Name the parasite shown.
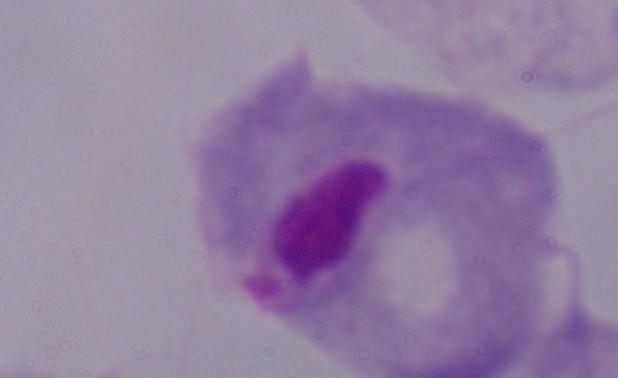

A trichomonad.

1000x magnification. Photomicrograph.